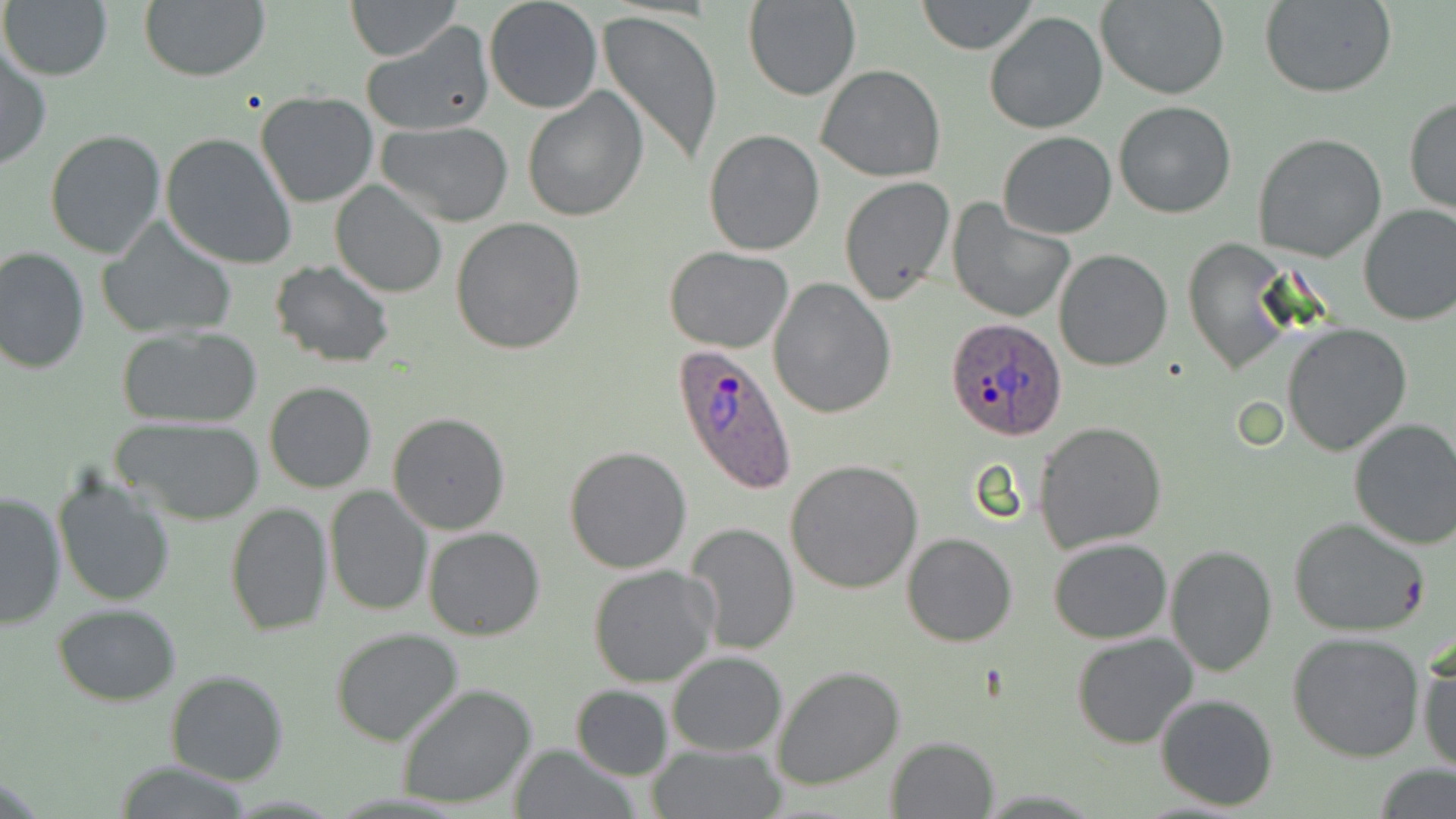 Approximate bounding boxes as named x1/y1/x2/y2 corners in pixels. Plasmodium ovale-infected red blood cell locations: (x1=944, y1=319, x2=1069, y2=441), (x1=672, y1=343, x2=798, y2=495). Uninfected red blood cell locations: (x1=0, y1=0, x2=113, y2=82), (x1=346, y1=0, x2=462, y2=61), (x1=483, y1=0, x2=602, y2=115), (x1=743, y1=0, x2=860, y2=101), (x1=916, y1=0, x2=1039, y2=54), (x1=1097, y1=0, x2=1230, y2=99), (x1=138, y1=1, x2=270, y2=82), (x1=1262, y1=1, x2=1398, y2=99), (x1=597, y1=9, x2=724, y2=169), (x1=984, y1=11, x2=1107, y2=135), (x1=362, y1=24, x2=496, y2=137), (x1=0, y1=47, x2=51, y2=170), (x1=815, y1=64, x2=948, y2=182), (x1=522, y1=87, x2=647, y2=222), (x1=256, y1=91, x2=379, y2=208), (x1=1403, y1=96, x2=1456, y2=216), (x1=1113, y1=101, x2=1237, y2=219), (x1=378, y1=120, x2=515, y2=225), (x1=706, y1=128, x2=823, y2=254), (x1=44, y1=130, x2=166, y2=259), (x1=161, y1=132, x2=297, y2=269), (x1=997, y1=132, x2=1116, y2=240), (x1=1252, y1=132, x2=1387, y2=261), (x1=839, y1=177, x2=956, y2=306), (x1=330, y1=182, x2=447, y2=298), (x1=948, y1=201, x2=1075, y2=322), (x1=1358, y1=203, x2=1456, y2=327), (x1=451, y1=219, x2=587, y2=356), (x1=99, y1=222, x2=237, y2=342), (x1=1185, y1=238, x2=1295, y2=374), (x1=664, y1=245, x2=794, y2=353), (x1=0, y1=246, x2=91, y2=374), (x1=1053, y1=248, x2=1174, y2=372), (x1=270, y1=260, x2=396, y2=368), (x1=767, y1=276, x2=894, y2=418), (x1=1282, y1=324, x2=1413, y2=456), (x1=116, y1=325, x2=264, y2=429), (x1=264, y1=380, x2=377, y2=494), (x1=388, y1=413, x2=511, y2=534), (x1=115, y1=417, x2=264, y2=526), (x1=1348, y1=417, x2=1456, y2=551), (x1=1034, y1=421, x2=1167, y2=553), (x1=564, y1=446, x2=693, y2=574), (x1=786, y1=459, x2=921, y2=593), (x1=52, y1=474, x2=176, y2=607), (x1=325, y1=486, x2=431, y2=616), (x1=0, y1=490, x2=67, y2=632), (x1=224, y1=502, x2=333, y2=636), (x1=1289, y1=518, x2=1431, y2=639), (x1=684, y1=523, x2=800, y2=655), (x1=422, y1=526, x2=545, y2=640), (x1=901, y1=532, x2=1018, y2=646), (x1=1047, y1=537, x2=1173, y2=643), (x1=1164, y1=545, x2=1278, y2=677), (x1=588, y1=563, x2=719, y2=687), (x1=53, y1=604, x2=182, y2=705), (x1=331, y1=627, x2=465, y2=746), (x1=1288, y1=630, x2=1427, y2=762), (x1=1071, y1=631, x2=1198, y2=749), (x1=1417, y1=644, x2=1456, y2=776), (x1=666, y1=651, x2=786, y2=757), (x1=772, y1=665, x2=904, y2=791), (x1=166, y1=669, x2=288, y2=786), (x1=397, y1=682, x2=537, y2=810), (x1=569, y1=684, x2=675, y2=780), (x1=1154, y1=693, x2=1280, y2=811), (x1=884, y1=736, x2=999, y2=819), (x1=506, y1=742, x2=637, y2=818), (x1=648, y1=743, x2=783, y2=818), (x1=113, y1=762, x2=253, y2=818), (x1=1374, y1=763, x2=1454, y2=817). Slide-level diagnosis: Plasmodium ovale. May-Grünwald-Giemsa-stained preparation. Thin blood film. One field of a larger specimen. Image is 1456×819 pixels. 1000x magnification. Light microscopy.